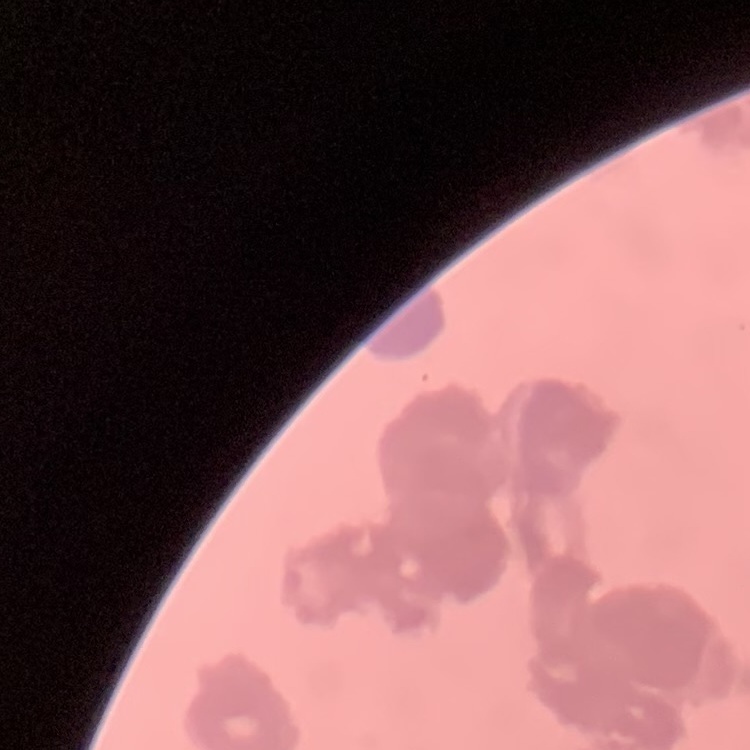

red blood cell morphology = rouleaux formation
stain = Field's or Giemsa
image type = one tile cut from a larger photomicrograph
preparation = thin blood film